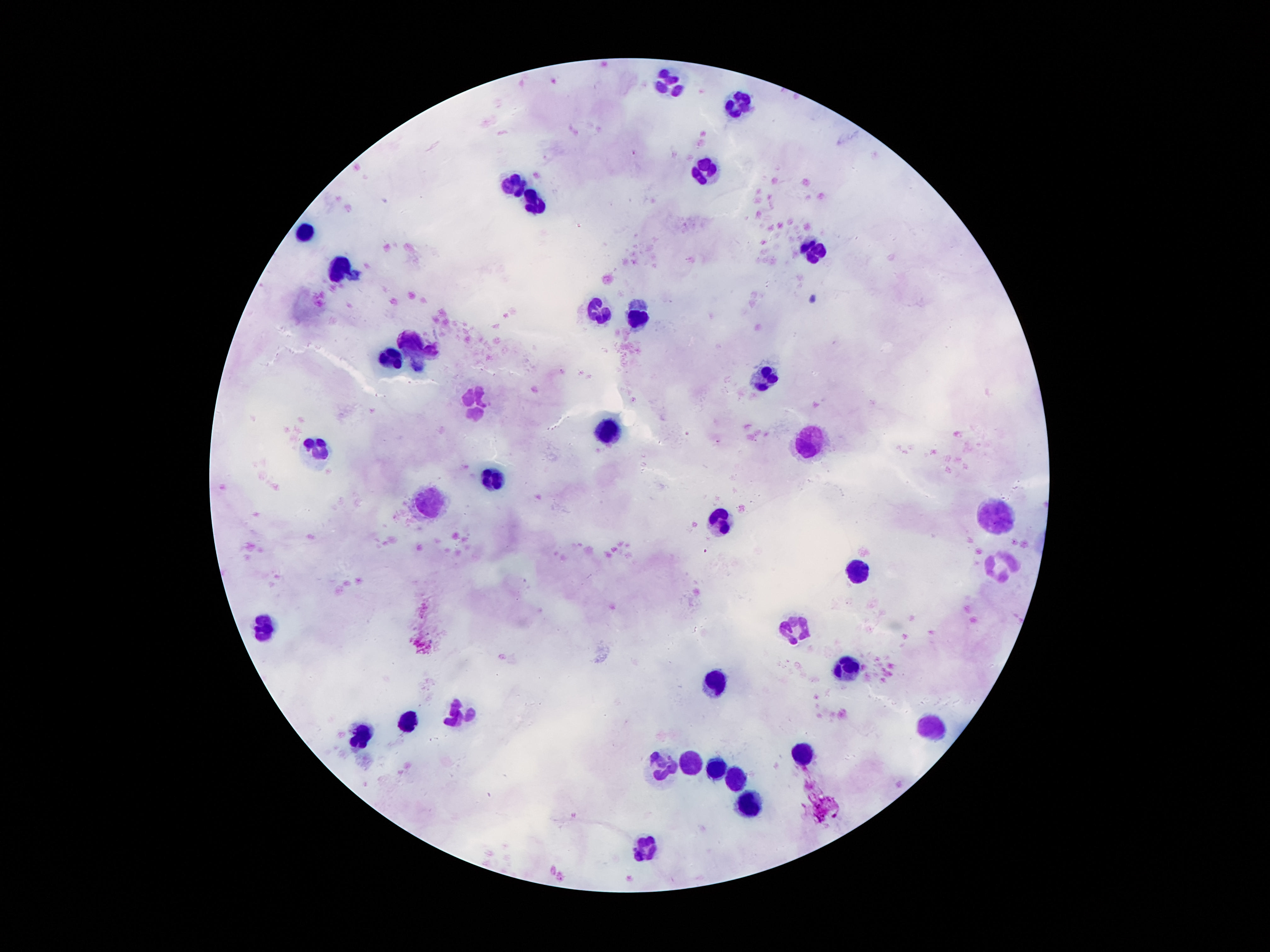
Approximate centers as [x, y] in pixels. Leukocyte locations: [668, 83], [740, 104], [704, 172], [514, 182], [534, 203], [303, 230], [809, 250], [339, 269], [598, 310], [640, 313], [407, 343], [389, 359], [765, 374], [475, 400], [609, 430], [811, 442], [316, 450], [491, 474], [434, 501], [994, 514], [718, 521], [1001, 566], [858, 573], [266, 629], [795, 630], [845, 668], [713, 680], [457, 714], [407, 721], [929, 727], [361, 739], [802, 755], [690, 763], [663, 766], [716, 768], [734, 780], [747, 804], [641, 847]. Giemsa stain. 100x magnification. Thick peripheral-blood smear. Photographed through the microscope eyepiece with a smartphone camera. Image is 1270×952 pixels. Patient malaria status: not infected. Single field of view.